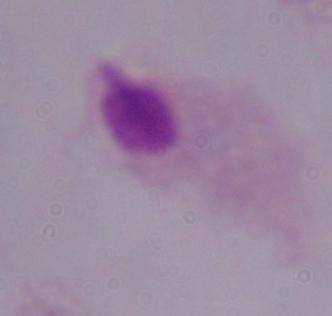

modality: photomicrograph
magnification: 1000x
identification: trichomonad